Assess the morphology of the erythrocytes.
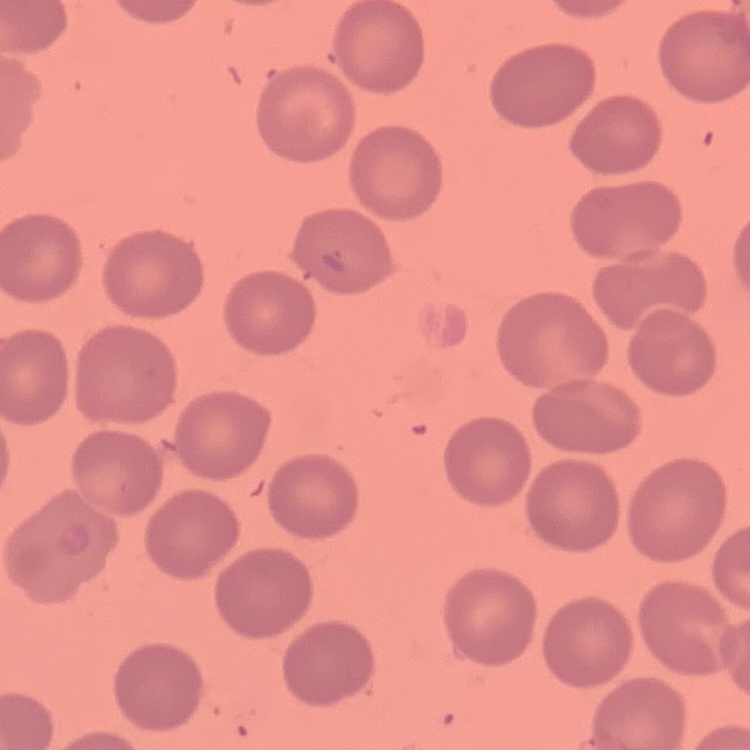
No rouleaux formation.

Summary:
  - Image type: square crop of a larger photomicrograph
  - Stain: Field's or Giemsa
  - Preparation: thin blood film